Assess this cell for malaria.
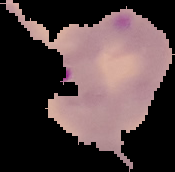

Parasitized.

preparation = thin blood smear
image size = 175×172 pixels
image type = segmented cell region with the area outside set to black